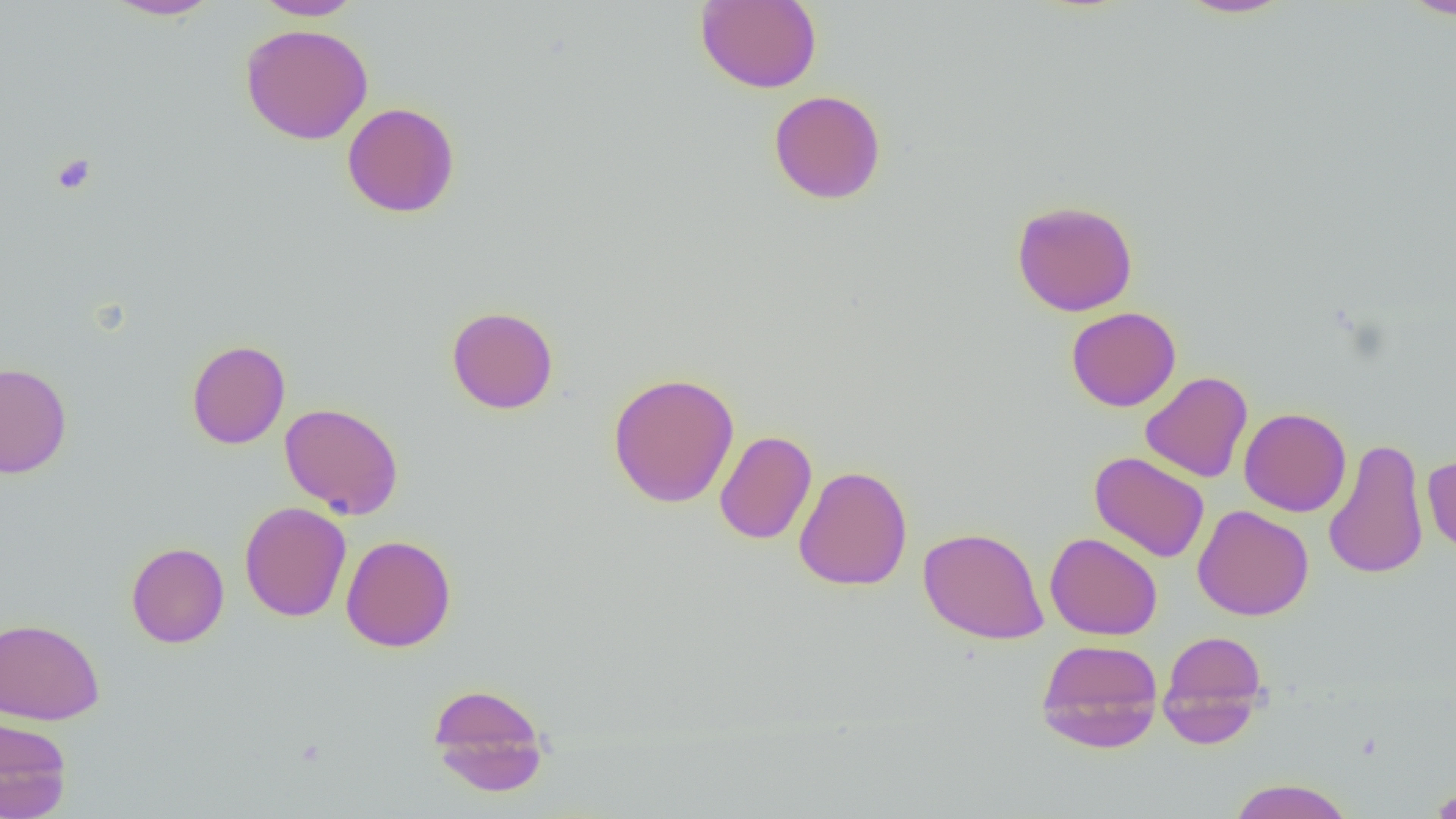

slide-level diagnosis = negative for blood parasites
modality = light microscopy
image size = 1456×819 pixels
platelet locations = approximate bounding boxes as [x1, y1, x2, y2] in pixels: [51, 153, 96, 196]
preparation = thin blood film
uninfected red blood cell locations = approximate bounding boxes as [x1, y1, x2, y2] in pixels: [104, 0, 221, 20], [252, 0, 365, 20], [1176, 0, 1294, 18], [1399, 0, 1456, 19], [695, 1, 822, 93], [240, 23, 374, 144], [769, 89, 886, 205], [342, 102, 460, 218], [1011, 199, 1138, 316], [446, 306, 559, 414], [1066, 307, 1181, 411], [186, 339, 291, 449], [0, 362, 72, 478], [1140, 371, 1253, 483], [607, 372, 740, 508], [279, 402, 404, 519], [1239, 407, 1351, 517], [714, 430, 817, 545], [1323, 437, 1429, 579], [1089, 451, 1210, 563], [1423, 453, 1455, 556], [794, 464, 912, 591], [239, 502, 351, 622], [1193, 504, 1314, 621], [918, 526, 1049, 645], [1045, 531, 1163, 640], [341, 534, 456, 652], [126, 542, 229, 648], [0, 617, 105, 725], [1158, 630, 1270, 746], [1035, 638, 1164, 753], [427, 683, 550, 796], [0, 716, 72, 819], [1226, 778, 1356, 819], [1426, 783, 1456, 818]
magnification = 1000x
field of view = single